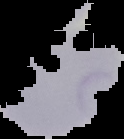

{
  "preparation": "thin blood film",
  "image_type": "segmented cell region on a black background",
  "malaria_status": "parasitized",
  "image_size": "124×139 pixels"
}